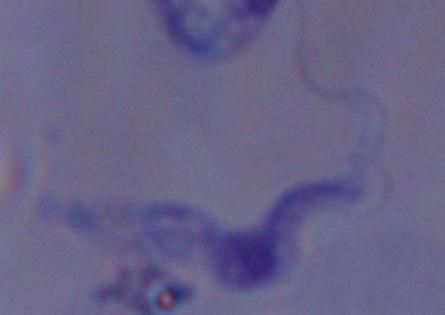
{
  "modality": "micrograph",
  "identification": "trypanosome",
  "magnification": "1000x"
}